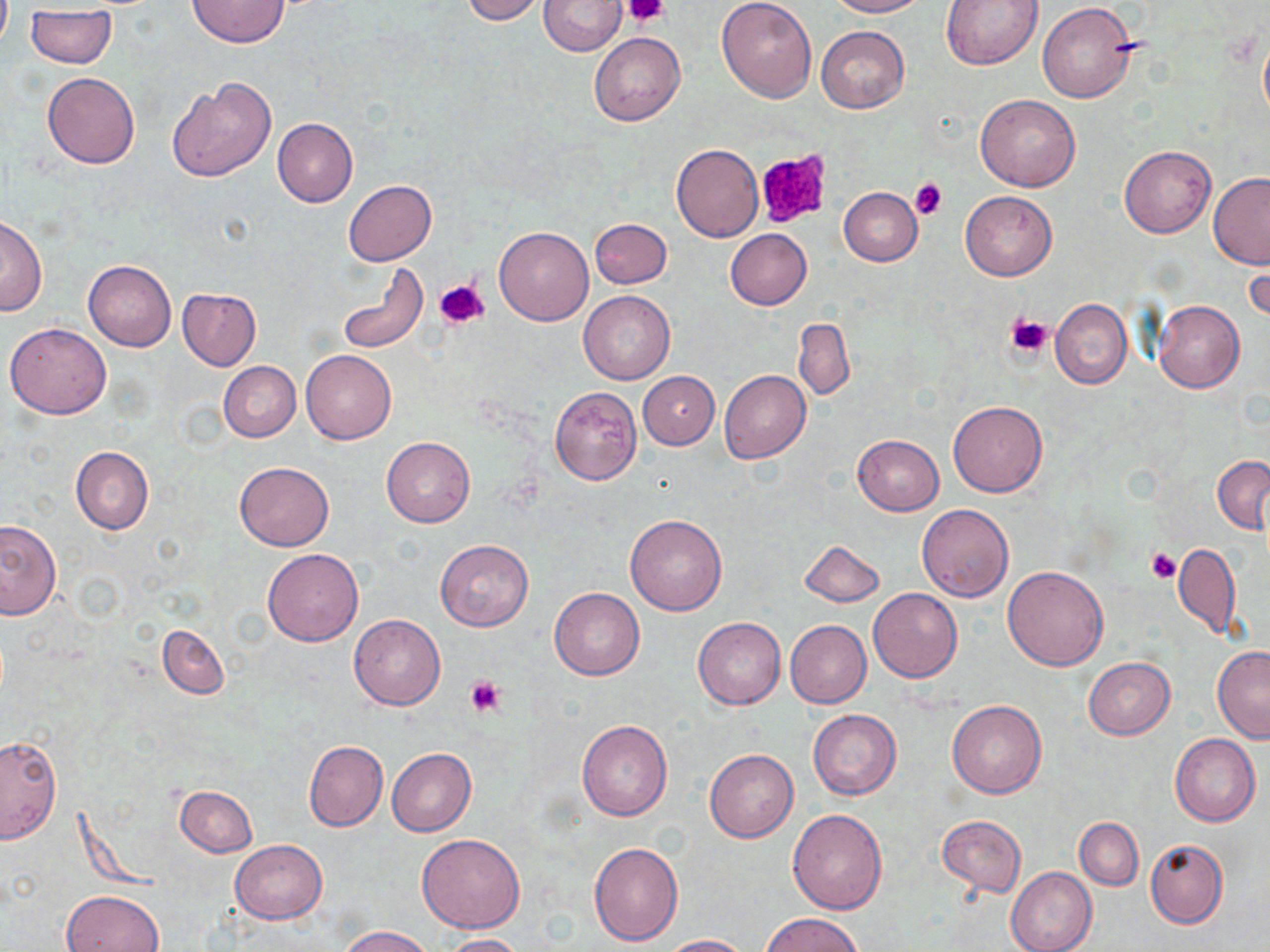

{
  "slide_level_diagnosis": "no evidence of blood parasites",
  "stain": "May-Grünwald-Giemsa",
  "modality": "optical microscopy",
  "magnification": "1000x",
  "uninfected_red_blood_cell_locations": "approximate bounding boxes as [x1, y1, x2, y2] in pixels: [459, 0, 547, 23], [540, 0, 624, 54], [827, 0, 931, 17], [938, 0, 1045, 69], [188, 1, 288, 47], [716, 1, 815, 102], [1037, 2, 1137, 102], [25, 9, 117, 69], [815, 25, 909, 114], [1258, 30, 1270, 126], [589, 32, 685, 126], [41, 73, 140, 168], [168, 78, 275, 181], [975, 94, 1080, 192], [272, 117, 357, 207], [672, 144, 763, 241], [1120, 145, 1216, 237], [1208, 172, 1270, 268], [343, 180, 437, 265], [839, 187, 922, 265], [959, 191, 1057, 281], [0, 216, 46, 316], [590, 218, 671, 288], [494, 226, 593, 325], [724, 228, 812, 309], [1244, 247, 1269, 326], [83, 260, 176, 351], [335, 260, 428, 355], [176, 289, 261, 371], [579, 291, 675, 384], [1050, 299, 1131, 388], [1152, 300, 1245, 394], [793, 318, 855, 402], [5, 322, 112, 418], [301, 350, 396, 444], [218, 361, 301, 442], [718, 369, 810, 463], [638, 371, 718, 449], [549, 386, 643, 485], [947, 399, 1049, 497], [853, 434, 944, 515], [382, 436, 475, 527], [70, 446, 153, 534], [1212, 455, 1270, 533], [233, 461, 334, 549], [916, 504, 1013, 602], [624, 515, 727, 616], [0, 520, 61, 618], [799, 539, 884, 607], [434, 540, 534, 631], [1172, 542, 1240, 640], [262, 549, 363, 646], [1002, 566, 1108, 670], [549, 588, 645, 680], [868, 588, 963, 682], [348, 614, 445, 710], [692, 617, 786, 709], [785, 620, 872, 707], [158, 625, 229, 699], [1212, 646, 1270, 742], [1083, 657, 1175, 739], [946, 700, 1047, 798], [807, 709, 901, 800], [576, 719, 673, 822], [1171, 734, 1260, 826], [0, 736, 61, 842], [303, 741, 387, 832], [387, 748, 477, 836], [705, 749, 798, 843], [174, 785, 258, 856], [788, 810, 887, 913], [937, 815, 1026, 897], [1074, 818, 1142, 889], [416, 834, 525, 934], [229, 839, 328, 924], [1145, 840, 1227, 929], [589, 841, 684, 945], [1005, 867, 1097, 952], [62, 889, 164, 952], [762, 912, 866, 951], [339, 925, 436, 952], [661, 933, 752, 952], [441, 934, 527, 952]",
  "preparation": "thin blood smear",
  "platelet_locations": "approximate bounding boxes as [x1, y1, x2, y2] in pixels: [623, 0, 670, 26], [756, 150, 830, 229], [910, 179, 946, 220], [435, 280, 491, 329], [1005, 314, 1053, 360], [1146, 548, 1180, 584], [462, 675, 505, 718]",
  "image_size": "1270×952 pixels",
  "field_of_view": "single"
}